Name the blood parasite species.
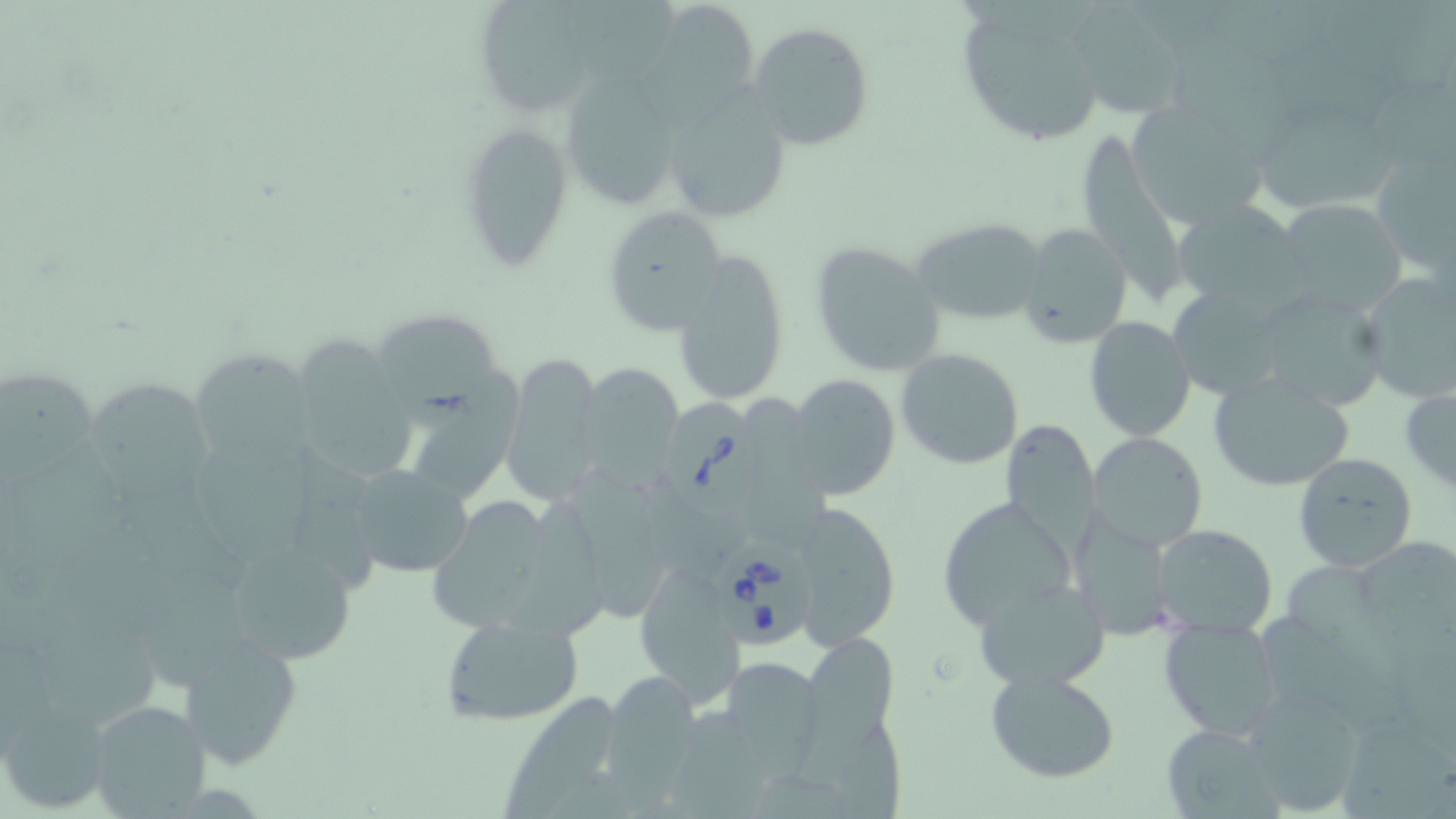

Babesia divergens.

Approximate bounding boxes as (x1,y1)-(x2,y2) corner pairs in pixels. Uninfected red blood cell locations: (565,0)-(682,81), (1072,2)-(1182,114), (954,3)-(1112,149), (648,5)-(762,107), (486,8)-(588,111), (747,21)-(874,152), (1170,48)-(1303,154), (1273,51)-(1399,138), (571,80)-(673,208), (1368,81)-(1456,173), (659,85)-(793,223), (1132,107)-(1265,226), (1262,118)-(1396,210), (456,121)-(572,270), (1081,134)-(1185,294), (1375,159)-(1456,276), (1171,199)-(1306,313), (1276,199)-(1408,317), (599,205)-(726,335), (910,217)-(1047,326), (1018,221)-(1133,348), (809,241)-(948,378), (672,252)-(792,409), (1355,268)-(1456,404), (1169,291)-(1277,393), (1266,295)-(1380,410), (371,313)-(503,432), (1084,316)-(1195,441), (285,338)-(420,485), (191,346)-(320,470), (895,348)-(1023,468), (499,354)-(604,504), (573,361)-(687,482), (1213,372)-(1352,491), (788,374)-(900,500), (1,376)-(96,487), (82,378)-(218,499), (1400,382)-(1456,494), (743,393)-(832,566), (399,394)-(520,506), (1000,419)-(1100,553), (1087,431)-(1208,554), (197,440)-(313,559), (6,444)-(136,568), (297,449)-(375,593), (1293,453)-(1417,570), (563,463)-(667,628), (344,464)-(473,579), (116,486)-(252,588), (647,494)-(749,578), (936,496)-(1076,632), (428,497)-(546,630), (504,500)-(608,639), (794,501)-(902,648), (1073,512)-(1171,640), (1155,523)-(1276,636), (209,530)-(369,667), (1359,535)-(1456,637), (151,561)-(247,692), (1284,562)-(1403,694), (635,563)-(747,707), (975,578)-(1111,691), (43,610)-(169,723), (1258,612)-(1406,737), (440,613)-(585,727), (1158,618)-(1285,742), (801,630)-(901,740), (177,634)-(302,771), (717,655)-(826,768), (985,669)-(1122,784), (599,671)-(709,802), (1240,689)-(1366,817), (502,692)-(615,819), (0,696)-(112,810), (82,698)-(213,819), (670,702)-(765,818), (795,712)-(908,819), (1161,724)-(1279,817), (1343,728)-(1456,819). Babesia divergens-infected red blood cell locations: (662,396)-(766,517), (715,543)-(814,648). Thin blood film. Light microscopy. Image is 1456×819 pixels. May-Grünwald-Giemsa-stained preparation. Single field of view. 1000x magnification.